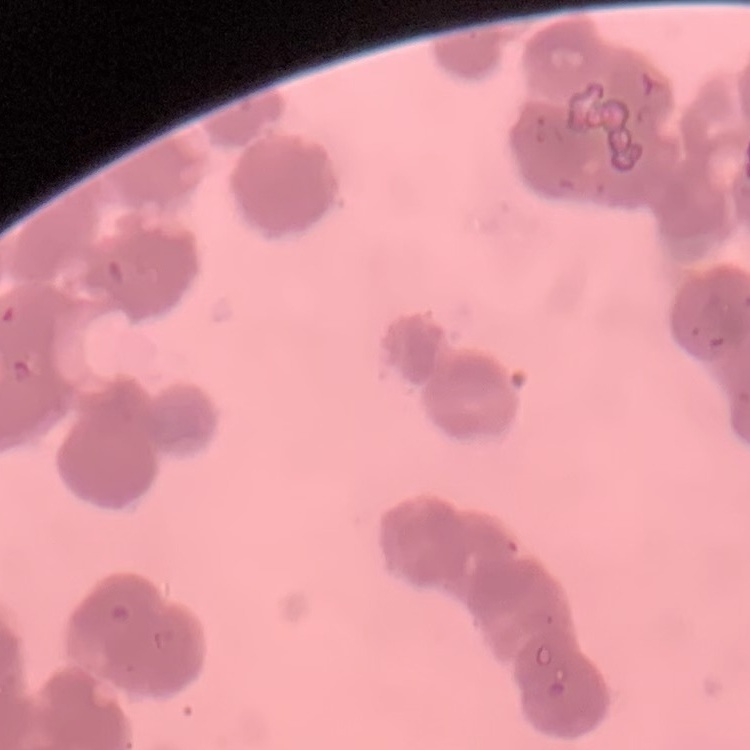
Summary:
  - Erythrocyte morphology: rouleaux formation
  - Image type: square crop of a larger photomicrograph
  - Preparation: thin peripheral smear
  - Stain: Field's or Giemsa